Outline every leukocyte.
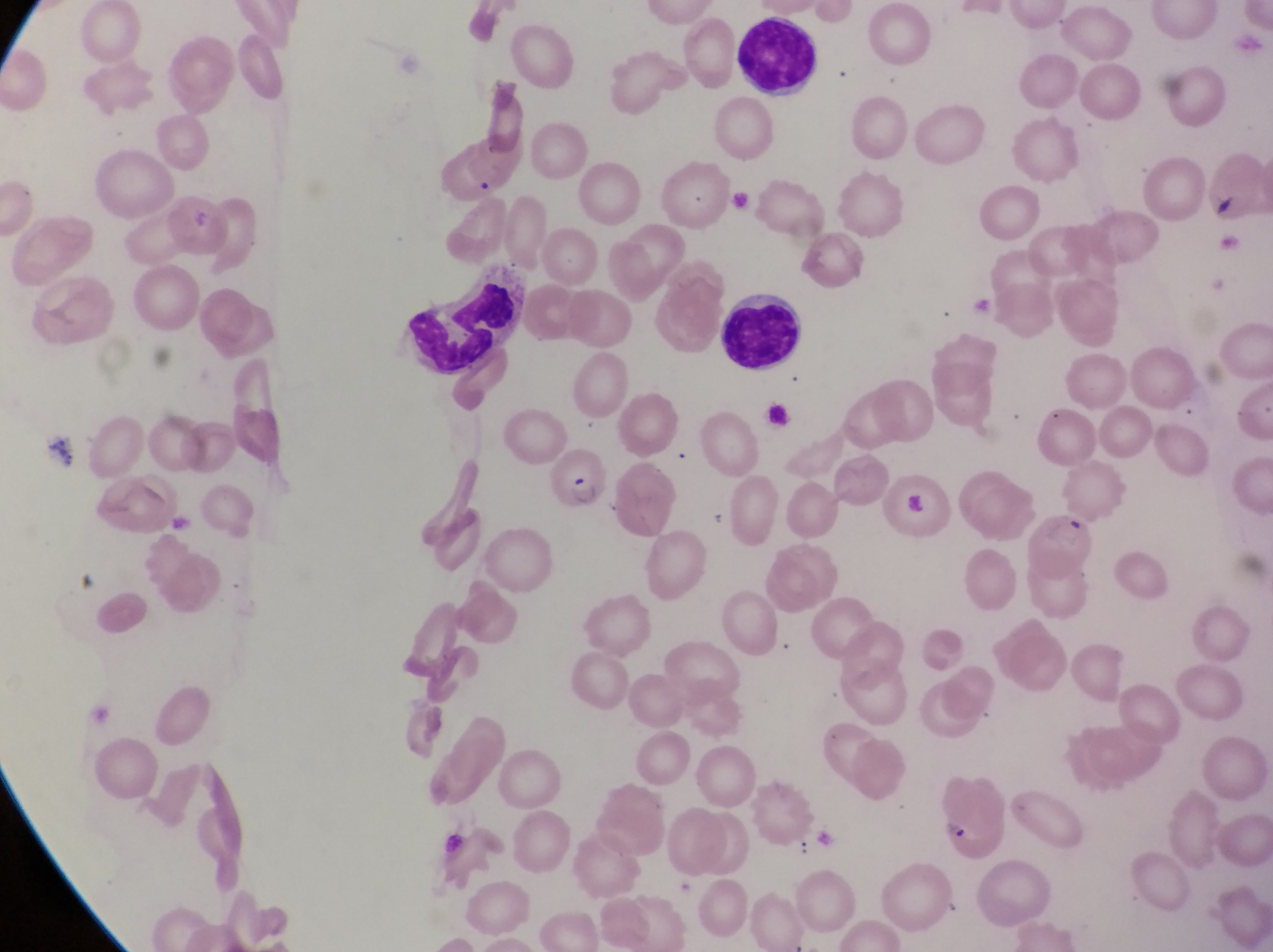

Approximate bounding boxes as [left, top, right, bottom] in pixels.
Leukocytes: [736, 13, 826, 96], [402, 280, 519, 377], [724, 292, 809, 372].

Parasitised red blood cell locations: [547, 445, 609, 503], [878, 465, 956, 543], [928, 774, 1010, 861]. Artifact (platelet-like body, stain precipitate, or debris) locations: [1211, 188, 1241, 220]. Captured by a smartphone held over the eyepiece of an Olympus CX-23 microscope. Thin blood film. At a magnification of 1000x. Image is 1273×952 pixels. One field of view. Collected in Uganda.